Give the position of every leukocyte visible.
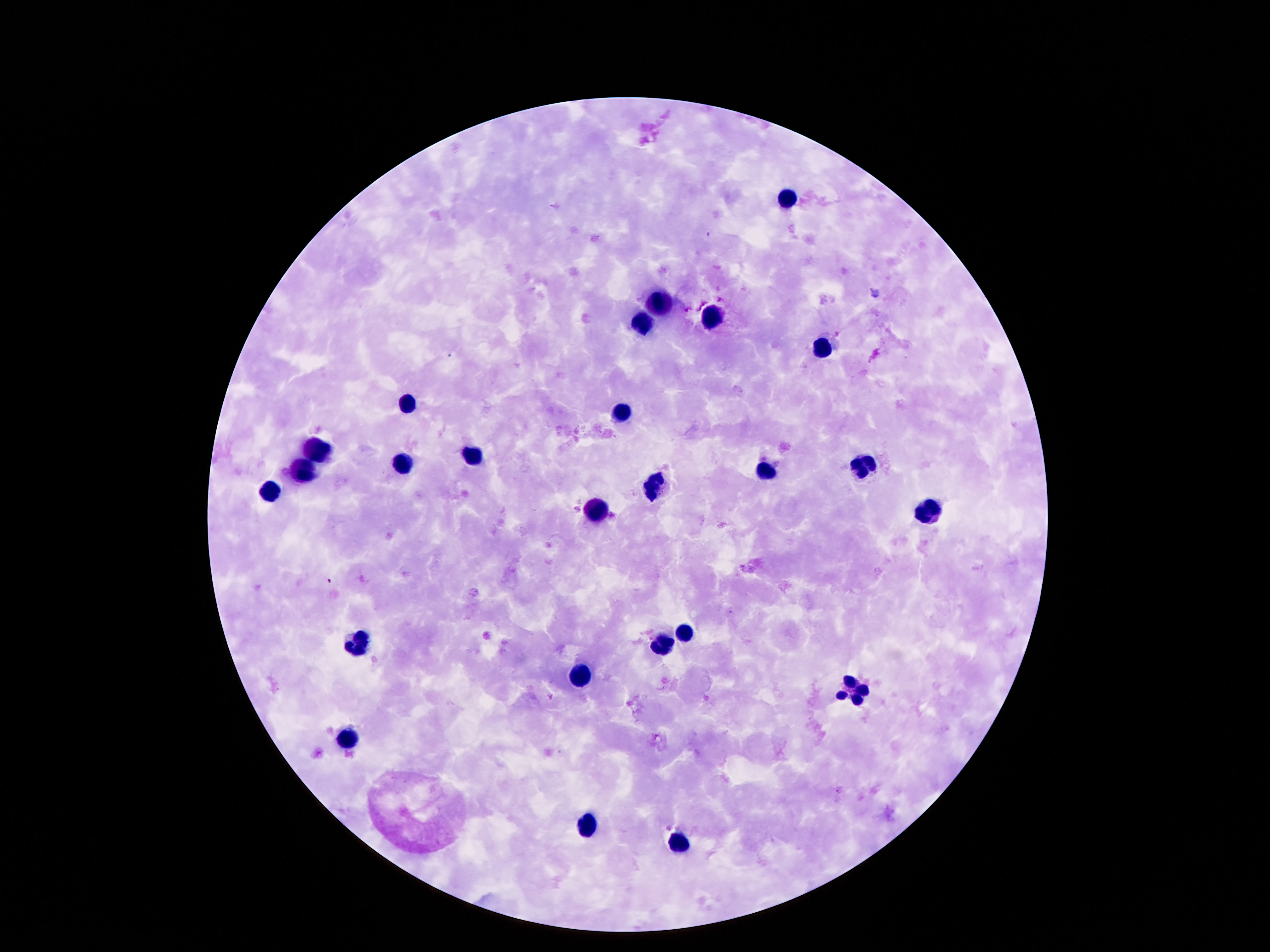
Approximate centers as (x, y) in pixels.
Leukocytes: (789, 199), (661, 304), (711, 320), (642, 325), (823, 348), (407, 402), (621, 414), (321, 451), (474, 455), (407, 465), (858, 469), (304, 472), (766, 474), (652, 486), (268, 490), (596, 509), (925, 509), (684, 631), (358, 641), (661, 647), (584, 674), (851, 690), (350, 739), (590, 829), (676, 844).

Image is 1270×952 pixels. Giemsa-stained preparation. 100x magnification. Thick blood film. Photographed through the microscope eyepiece with a smartphone camera. One field from this slide. Patient malaria status: negative.